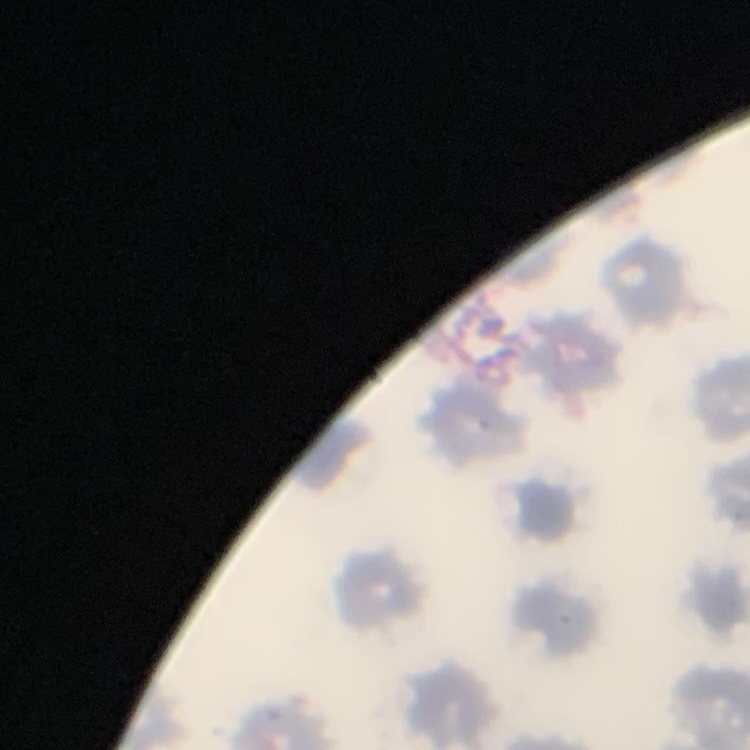
Summary:
  - Red blood cell morphology: no rouleaux formation
  - Image type: one tile cut from a larger photomicrograph
  - Stain: Field's or Giemsa
  - Preparation: thin peripheral smear